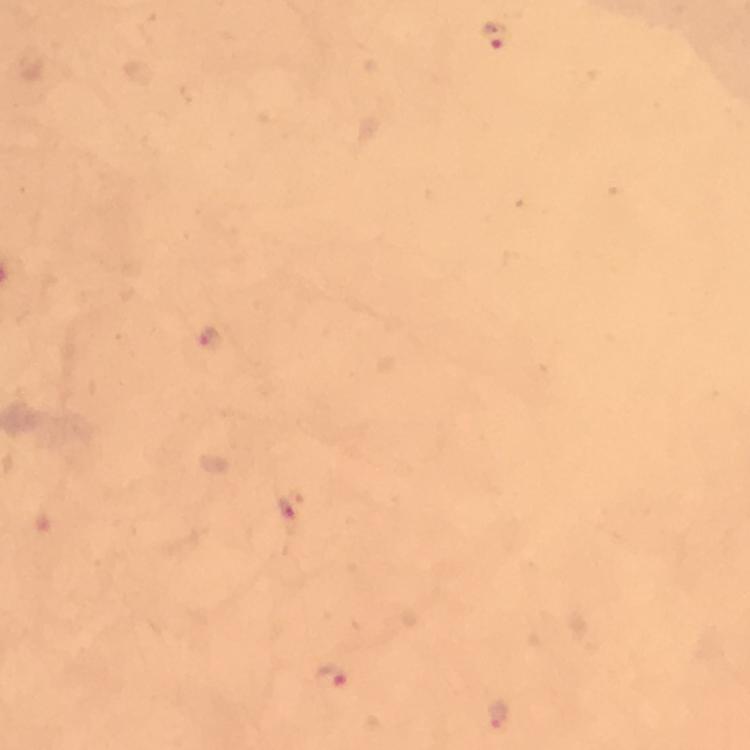
{
  "immersion_oil": "used",
  "magnification": "100x",
  "plasmodium_parasite_locations": "approximate object centers, in pixels from the top-left corner: (x=494, y=37), (x=208, y=338), (x=286, y=509), (x=332, y=677), (x=497, y=714)",
  "image_size": "750×750 pixels",
  "cropped_from": "one field of view",
  "stain": "Giemsa",
  "preparation": "thick smear",
  "context": "from a diagnostic examination for malaria",
  "capture": "smartphone mounted on the microscope"
}